Classify this cell by malaria status.
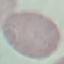

Uninfected.

Giemsa stain. Thin blood smear. Acquired by smartphone through the microscope eyepiece. Cell patch, automatically extracted from a larger field of view and resized to 64 × 64 pixels.